Comment on the morphology of the erythrocytes.
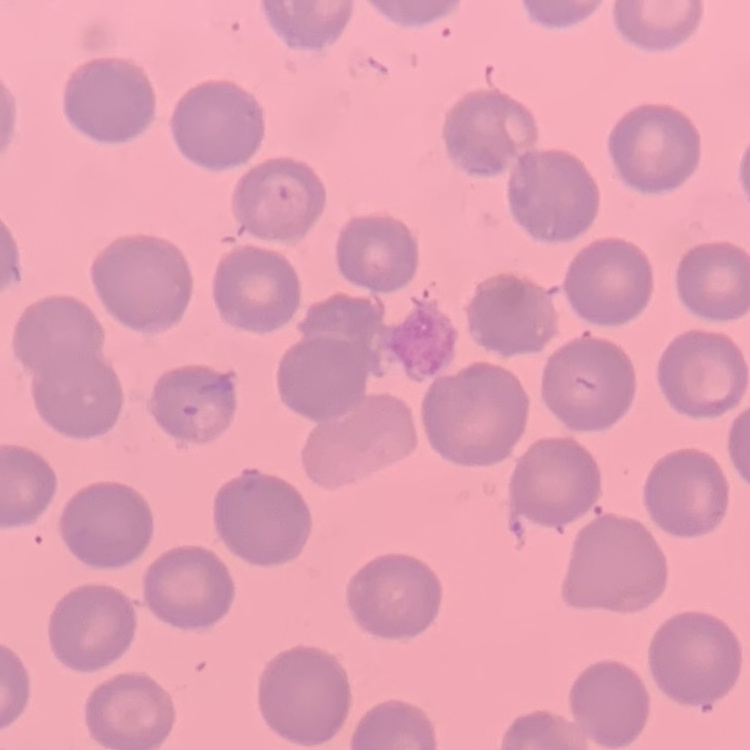
No rouleaux formation.

image type = square crop of a larger photomicrograph
preparation = thin peripheral smear
stain = Field's or Giemsa